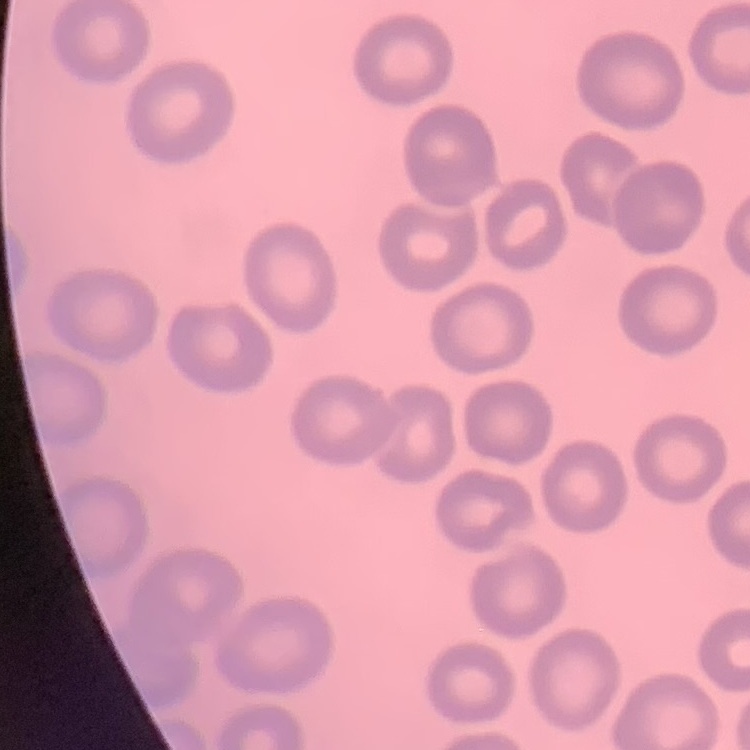
Summary:
  - Red blood cell morphology: no rouleaux formation
  - Image type: square crop of a larger photomicrograph
  - Stain: Field's or Giemsa
  - Preparation: thin blood film